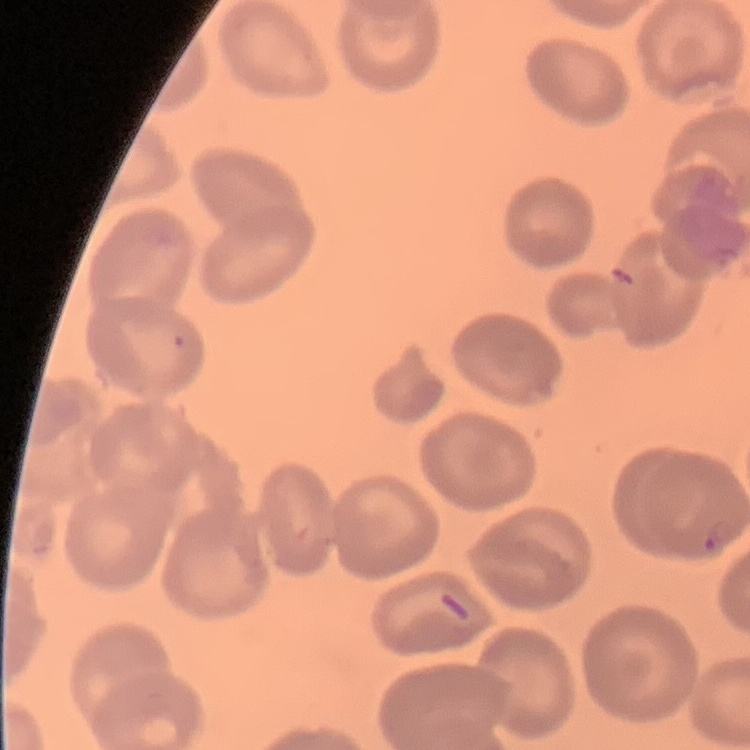

Summary:
  - Red blood cell morphology: no rouleaux formation
  - Image type: one tile cut from a larger photomicrograph
  - Stain: Field's or Giemsa
  - Preparation: thin peripheral smear